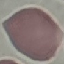
malaria status = uninfected
preparation = thin smear
image type = cell patch, automatically extracted from a larger field of view and resized to 64 × 64 pixels
capture = smartphone through the microscope eyepiece
stain = Giemsa